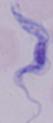 Captured at 1000x magnification. A trypanosome is shown. Micrograph.